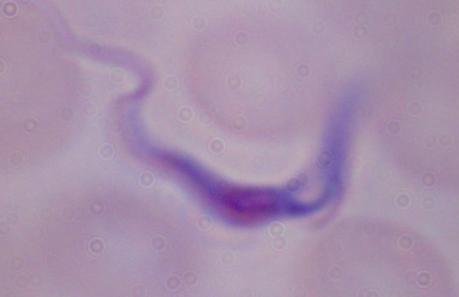
magnification = 1000x
identification = trypanosome
modality = photomicrograph